Assess this cell for malaria.
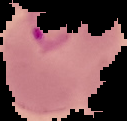

Parasitized.

From a thin blood film. The area outside the segmented cell region is set to black. Image is 127×121 pixels.